Assess this cell for malaria.
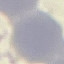
It is uninfected.

image type = automatically extracted cell patch, resized to 64 × 64 pixels
preparation = thin blood smear
capture = smartphone through the microscope eyepiece
stain = Giemsa